Identify the cell.
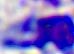
This is a leukocyte.

400x magnification. Photomicrograph.